Locate every blood parasite and identify its species.
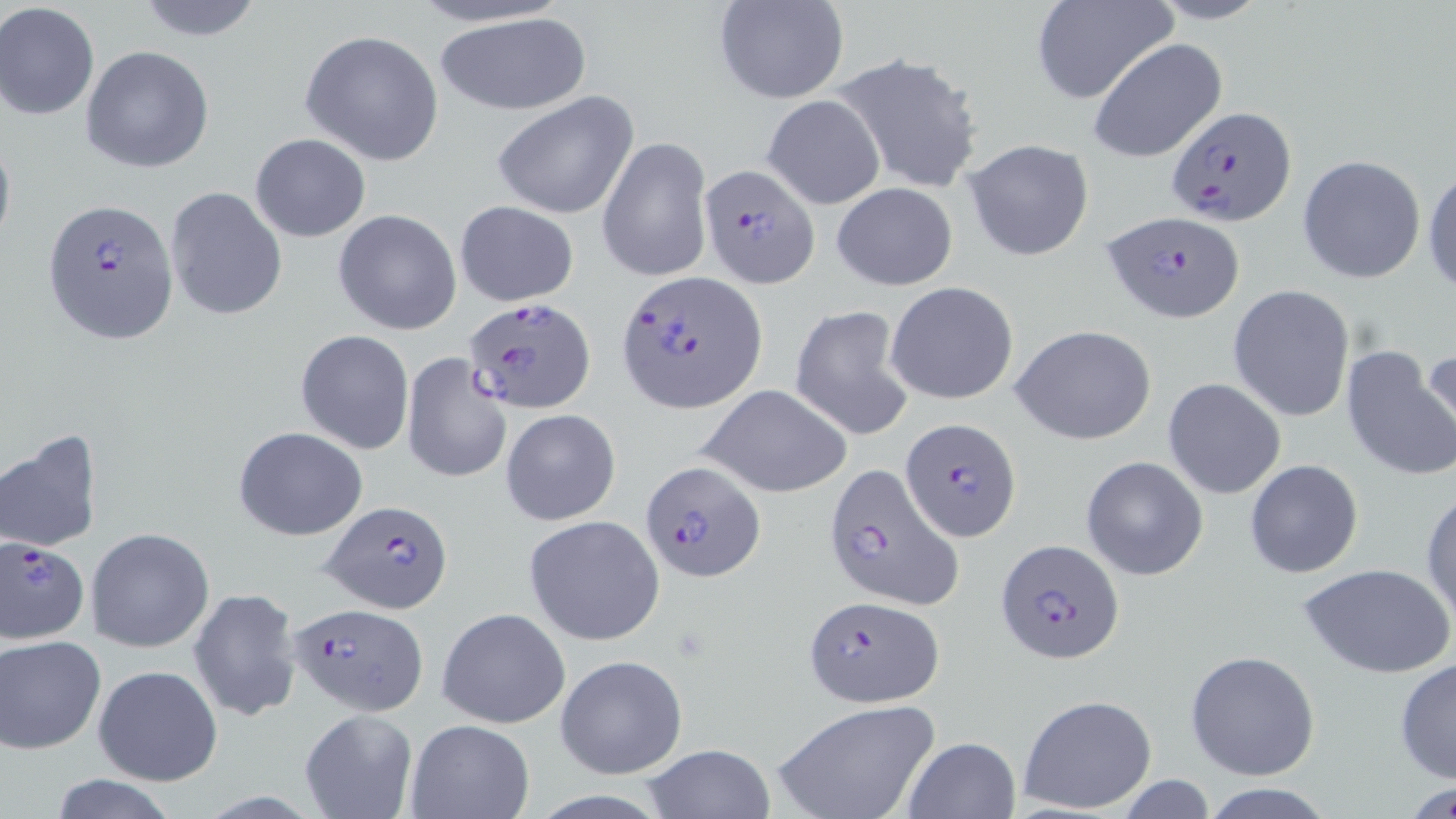

Approximate bounding boxes as named x1/y1/x2/y2 corners in pixels.
Plasmodium falciparum-infected red blood cells: (x1=1164, y1=105, x2=1298, y2=226), (x1=697, y1=162, x2=820, y2=287), (x1=44, y1=198, x2=179, y2=344), (x1=1103, y1=213, x2=1243, y2=323), (x1=616, y1=273, x2=768, y2=415), (x1=461, y1=297, x2=594, y2=416), (x1=902, y1=417, x2=1022, y2=539), (x1=641, y1=458, x2=764, y2=581), (x1=821, y1=463, x2=962, y2=613), (x1=321, y1=499, x2=451, y2=613), (x1=2, y1=536, x2=91, y2=644), (x1=996, y1=539, x2=1126, y2=664), (x1=803, y1=595, x2=943, y2=708), (x1=287, y1=602, x2=428, y2=714).
No Plasmodium ovale, Plasmodium malariae, Plasmodium vivax, Babesia divergens, or Trypanosoma brucei observed.

Uninfected red blood cell locations: (x1=133, y1=0, x2=267, y2=41), (x1=1030, y1=0, x2=1177, y2=105), (x1=715, y1=1, x2=848, y2=104), (x1=0, y1=3, x2=100, y2=121), (x1=432, y1=10, x2=594, y2=116), (x1=299, y1=29, x2=444, y2=165), (x1=1087, y1=38, x2=1227, y2=163), (x1=81, y1=45, x2=215, y2=174), (x1=832, y1=52, x2=986, y2=194), (x1=492, y1=91, x2=639, y2=219), (x1=762, y1=95, x2=886, y2=210), (x1=0, y1=127, x2=16, y2=262), (x1=250, y1=133, x2=370, y2=242), (x1=596, y1=134, x2=714, y2=284), (x1=962, y1=137, x2=1096, y2=262), (x1=1297, y1=155, x2=1426, y2=284), (x1=1423, y1=165, x2=1456, y2=298), (x1=831, y1=182, x2=957, y2=290), (x1=165, y1=185, x2=287, y2=321), (x1=454, y1=200, x2=579, y2=307), (x1=334, y1=209, x2=462, y2=335), (x1=885, y1=281, x2=1020, y2=406), (x1=1229, y1=286, x2=1354, y2=422), (x1=789, y1=305, x2=915, y2=439), (x1=1011, y1=324, x2=1157, y2=445), (x1=296, y1=330, x2=416, y2=454), (x1=1409, y1=343, x2=1456, y2=472), (x1=1340, y1=345, x2=1454, y2=482), (x1=400, y1=352, x2=513, y2=486), (x1=1162, y1=378, x2=1287, y2=500), (x1=698, y1=384, x2=853, y2=498), (x1=502, y1=408, x2=620, y2=525), (x1=232, y1=426, x2=367, y2=541), (x1=1, y1=429, x2=103, y2=553), (x1=1081, y1=456, x2=1208, y2=580), (x1=1243, y1=459, x2=1363, y2=577), (x1=1422, y1=489, x2=1456, y2=624), (x1=523, y1=514, x2=665, y2=645), (x1=86, y1=527, x2=214, y2=653), (x1=1298, y1=563, x2=1454, y2=679), (x1=189, y1=587, x2=301, y2=722), (x1=435, y1=608, x2=569, y2=728), (x1=2, y1=636, x2=106, y2=753), (x1=1185, y1=649, x2=1320, y2=780), (x1=555, y1=655, x2=688, y2=780), (x1=1393, y1=658, x2=1456, y2=783), (x1=92, y1=664, x2=221, y2=785), (x1=1017, y1=693, x2=1157, y2=815), (x1=771, y1=698, x2=940, y2=819), (x1=299, y1=708, x2=417, y2=819), (x1=404, y1=718, x2=533, y2=819), (x1=902, y1=736, x2=1019, y2=819), (x1=641, y1=744, x2=776, y2=818), (x1=43, y1=776, x2=183, y2=819), (x1=1403, y1=779, x2=1454, y2=817), (x1=1193, y1=782, x2=1340, y2=817). Slide-level diagnosis: Plasmodium falciparum. Optical microscopy. Captured at 1000x magnification. May-Grünwald-Giemsa stain. Thin blood smear. Image is 1456×819 pixels. One field of a larger specimen.